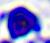
Summary:
  - Modality: micrograph
  - Magnification: 400x
  - Identification: leukocyte